Outline each blood parasite and name the species.
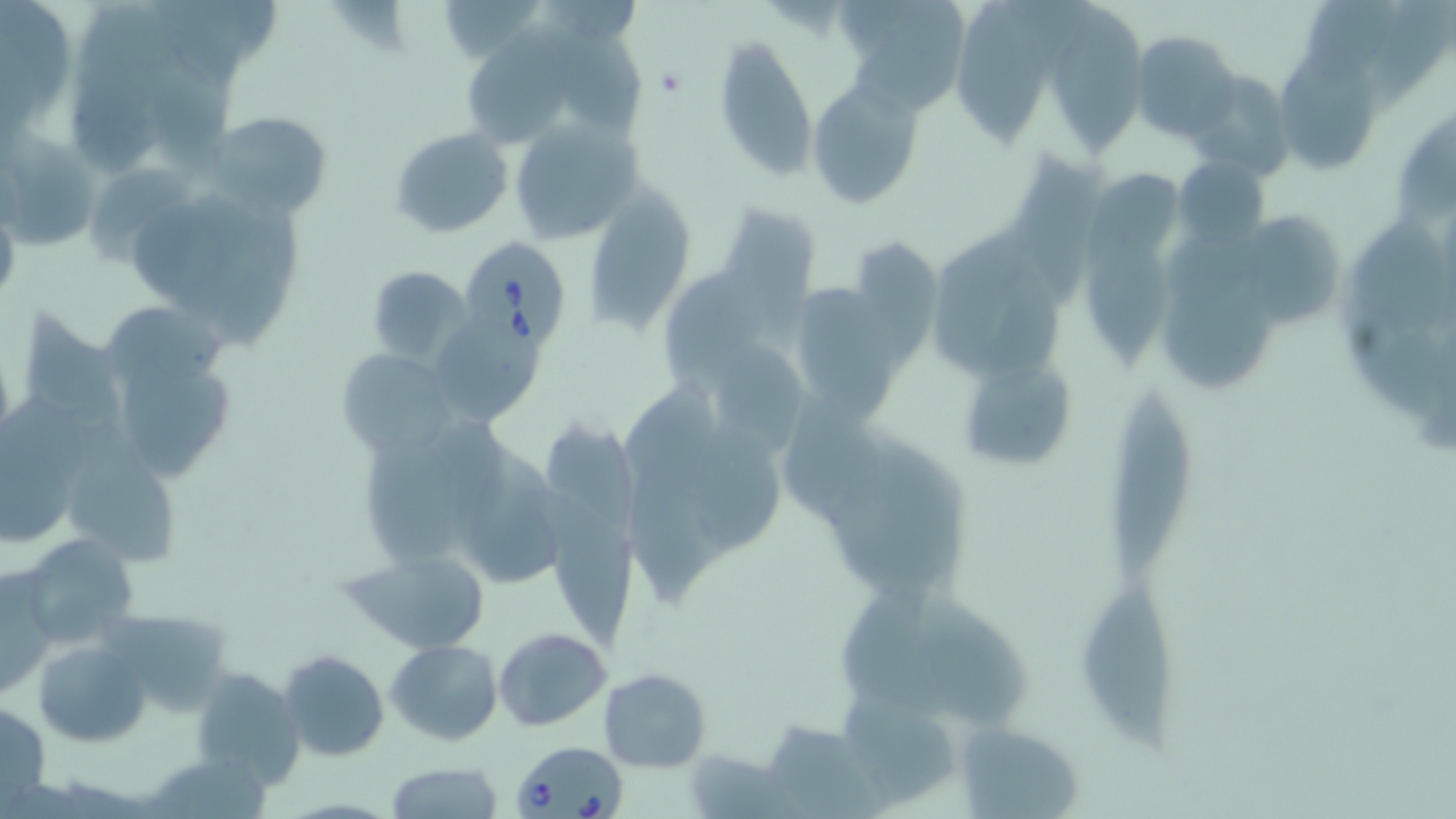

Approximate bounding boxes as named x1/y1/x2/y2 corners in pixels.
Babesia divergens-infected red blood cells: (x1=459, y1=237, x2=573, y2=346), (x1=511, y1=739, x2=629, y2=819).
No Plasmodium falciparum, Plasmodium ovale, Plasmodium malariae, Plasmodium vivax, or Trypanosoma brucei observed.

Platelet locations: (x1=654, y1=66, x2=688, y2=99). Uninfected red blood cell locations: (x1=156, y1=0, x2=245, y2=92), (x1=430, y1=0, x2=547, y2=64), (x1=543, y1=0, x2=641, y2=50), (x1=836, y1=0, x2=968, y2=115), (x1=0, y1=2, x2=68, y2=108), (x1=77, y1=3, x2=193, y2=93), (x1=1062, y1=4, x2=1150, y2=160), (x1=957, y1=7, x2=1058, y2=150), (x1=459, y1=24, x2=581, y2=141), (x1=551, y1=27, x2=639, y2=131), (x1=1131, y1=32, x2=1241, y2=143), (x1=714, y1=33, x2=818, y2=180), (x1=1284, y1=51, x2=1382, y2=170), (x1=153, y1=65, x2=234, y2=174), (x1=73, y1=69, x2=166, y2=170), (x1=1185, y1=70, x2=1297, y2=181), (x1=806, y1=78, x2=922, y2=208), (x1=1401, y1=107, x2=1456, y2=222), (x1=209, y1=109, x2=335, y2=222), (x1=504, y1=117, x2=644, y2=246), (x1=390, y1=128, x2=513, y2=238), (x1=0, y1=134, x2=100, y2=253), (x1=1011, y1=149, x2=1100, y2=308), (x1=1174, y1=155, x2=1271, y2=249), (x1=87, y1=159, x2=191, y2=266), (x1=586, y1=180, x2=693, y2=336), (x1=133, y1=205, x2=230, y2=305), (x1=717, y1=205, x2=818, y2=355), (x1=1251, y1=213, x2=1344, y2=329), (x1=1352, y1=213, x2=1451, y2=334), (x1=926, y1=220, x2=1029, y2=375), (x1=1090, y1=230, x2=1177, y2=376), (x1=1169, y1=231, x2=1260, y2=306), (x1=857, y1=236, x2=942, y2=372), (x1=366, y1=266, x2=472, y2=366), (x1=665, y1=269, x2=766, y2=387), (x1=978, y1=278, x2=1066, y2=379), (x1=799, y1=284, x2=890, y2=418), (x1=1164, y1=290, x2=1278, y2=387), (x1=101, y1=305, x2=229, y2=384), (x1=25, y1=306, x2=119, y2=419), (x1=439, y1=320, x2=537, y2=424), (x1=1346, y1=322, x2=1441, y2=415), (x1=715, y1=343, x2=804, y2=458), (x1=120, y1=346, x2=237, y2=481), (x1=335, y1=346, x2=458, y2=457), (x1=964, y1=357, x2=1079, y2=475), (x1=617, y1=380, x2=721, y2=490), (x1=771, y1=381, x2=879, y2=522), (x1=1104, y1=386, x2=1197, y2=582), (x1=694, y1=410, x2=780, y2=555), (x1=68, y1=417, x2=178, y2=565), (x1=543, y1=421, x2=648, y2=530), (x1=830, y1=433, x2=967, y2=594), (x1=464, y1=440, x2=563, y2=582), (x1=357, y1=448, x2=463, y2=563), (x1=0, y1=449, x2=78, y2=548), (x1=632, y1=469, x2=725, y2=598), (x1=534, y1=486, x2=636, y2=651), (x1=16, y1=532, x2=141, y2=648), (x1=344, y1=546, x2=494, y2=656), (x1=0, y1=568, x2=58, y2=705), (x1=1077, y1=583, x2=1185, y2=764), (x1=842, y1=587, x2=951, y2=719), (x1=916, y1=596, x2=1036, y2=728), (x1=109, y1=614, x2=227, y2=714), (x1=495, y1=629, x2=612, y2=730), (x1=387, y1=638, x2=502, y2=745), (x1=35, y1=639, x2=152, y2=747), (x1=278, y1=649, x2=389, y2=761), (x1=597, y1=667, x2=712, y2=771), (x1=189, y1=668, x2=303, y2=788), (x1=846, y1=694, x2=957, y2=804), (x1=0, y1=699, x2=51, y2=812), (x1=758, y1=721, x2=879, y2=817), (x1=955, y1=722, x2=1087, y2=815), (x1=685, y1=747, x2=787, y2=817), (x1=153, y1=754, x2=274, y2=819), (x1=385, y1=761, x2=505, y2=817). Slide-level diagnosis: Babesia divergens. Single field of view. Optical microscopy. 1000x magnification. Image is 1456×819 pixels. Thin blood film. May-Grünwald-Giemsa-stained preparation.